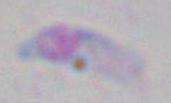
magnification = 1000x
modality = micrograph
identification = Toxoplasma gondii